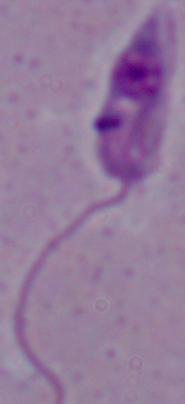

magnification: 1000x
modality: photomicrograph
identification: Leishmania